Point out each Plasmodium parasite.
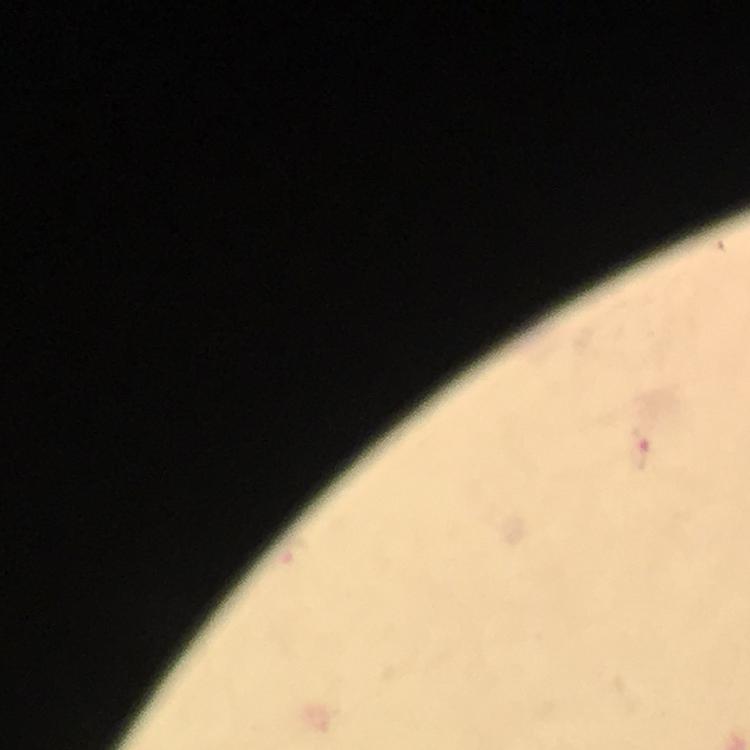
Approximate centers as [x, y] in pixels.
Plasmodium parasites: [637, 452].

image size = 750×750 pixels
cropped from = a single field of view
stain = Giemsa
magnification = 100x
preparation = thick smear
immersion oil = applied
context = from a malaria diagnostic workup
capture = smartphone camera through the microscope